Assess this cell for malaria.
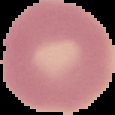

Uninfected.

image type = cell region segmented out of the field of view; surrounding area masked to black
preparation = thin blood film
image size = 115×115 pixels